Assess this cell for malaria.
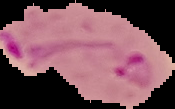
It is parasitized.

Image is 175×109 pixels. Cell region segmented out of the field of view; the surrounding area is masked to black. From a thin blood film.